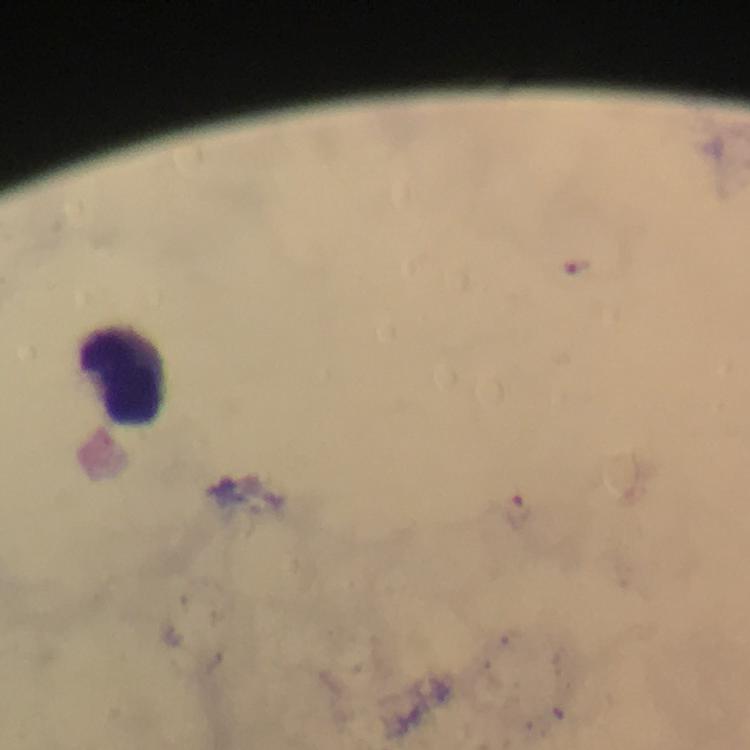
stain: Giemsa
cropped_from: a single field of view
preparation: thick blood smear
image_size: 750×750 pixels
plasmodium_parasite_locations: 'approximate centers as [x, y] in pixels: [577, 267], [519, 509]'
capture: smartphone camera through the microscope
context: from a diagnostic examination for malaria
magnification: 100x
immersion_oil: used
leukocyte_locations: 'approximate centers as [x, y] in pixels: [129, 377]'